Locate every leukocyte (white blood cell).
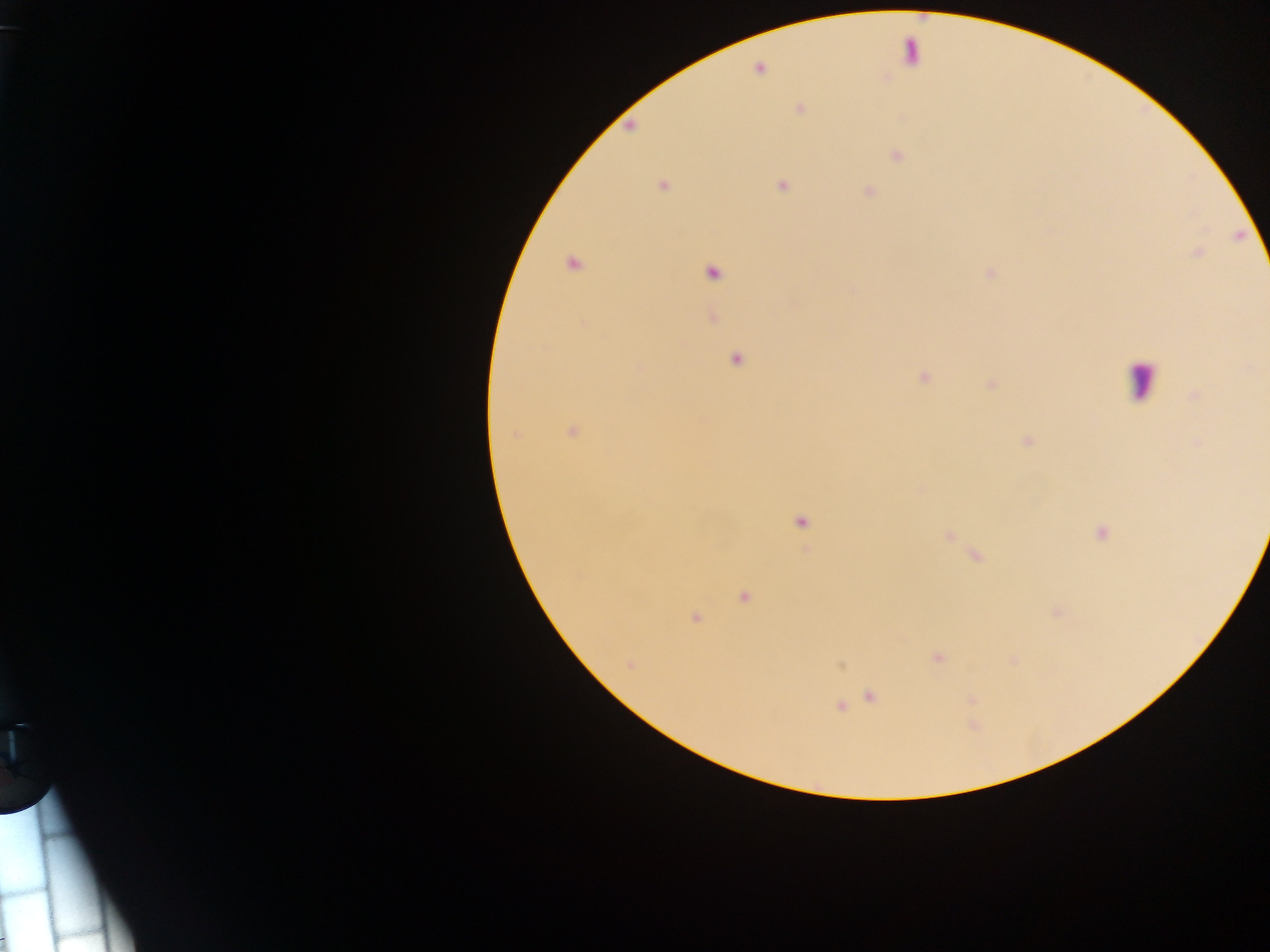

Approximate centers as x y in pixels.
Leukocytes: 1144 387.

Malaria parasite locations: 800 108; 630 127; 895 153; 662 184; 783 185; 867 191; 570 263; 988 272; 736 359; 925 376; 573 431; 802 521; 1101 533; 743 596; 696 616; 841 666; 871 696; 842 706; 6 939. Image is 1270×952 pixels. Thick blood smear. Single field of view. Collected in Ghana. Photographed through a microscope with a mobile-phone camera.